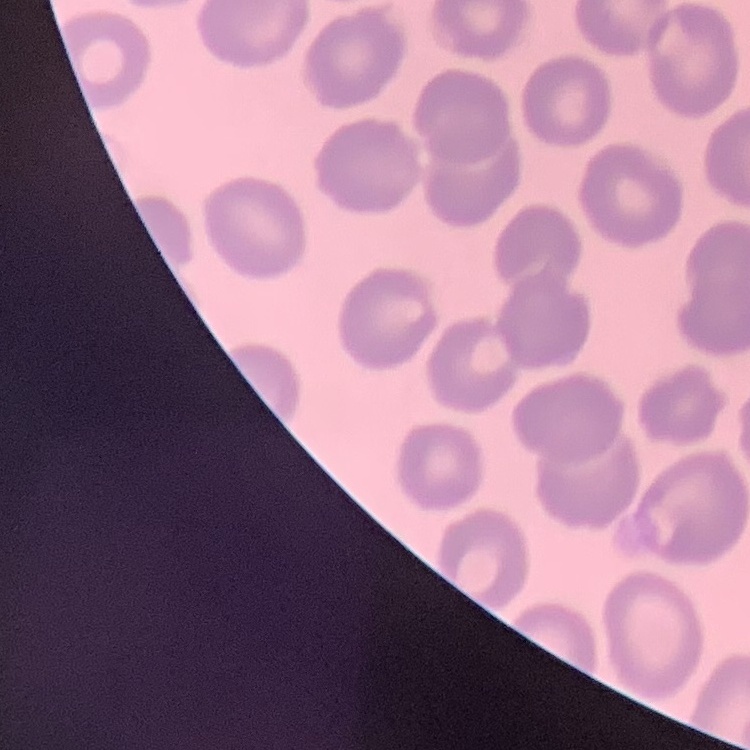
erythrocyte morphology = no rouleaux formation
preparation = thin peripheral smear
stain = Field's or Giemsa
image type = one tile cut from a larger photomicrograph